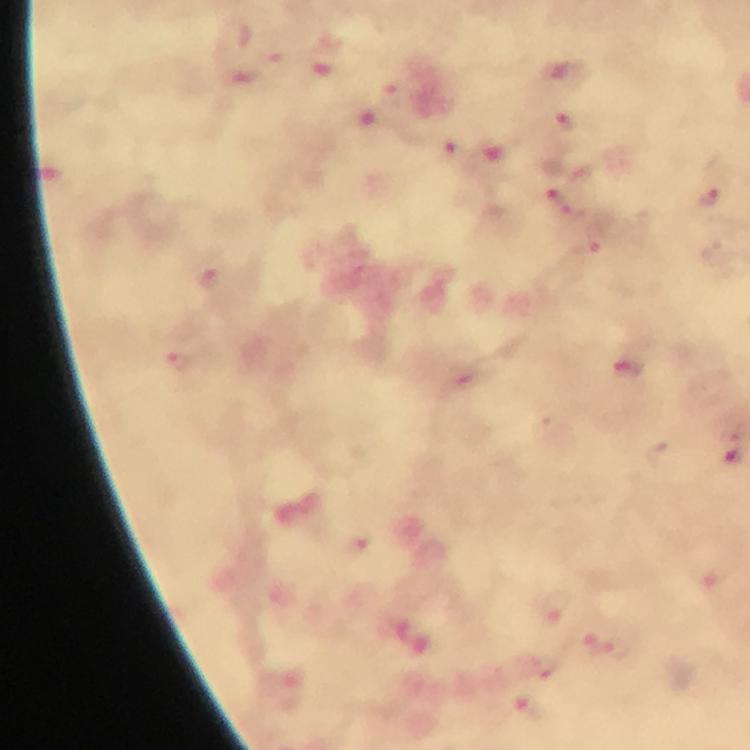

Approximate centers as {x, y} in pixels.
Summary:
  - Malaria parasite locations: {564, 120}, {708, 193}, {561, 194}, {576, 211}, {585, 248}, {632, 371}, {555, 605}, {582, 640}, {621, 647}, {540, 714}
  - Capture: smartphone photograph through a microscope
  - Context: from a malaria diagnostic workup
  - Magnification: 100x
  - Preparation: thick smear
  - Stain: Giemsa
  - Immersion oil: used
  - Cropped from: a single field of view
  - Image size: 750×750 pixels